State which parasite is depicted.
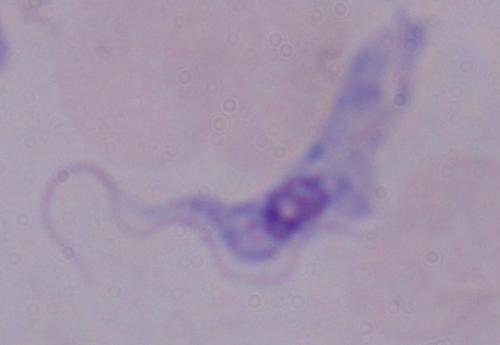
A trypanosome.

{
  "magnification": "1000x",
  "modality": "photomicrograph"
}